Locate every blood parasite and identify its species.
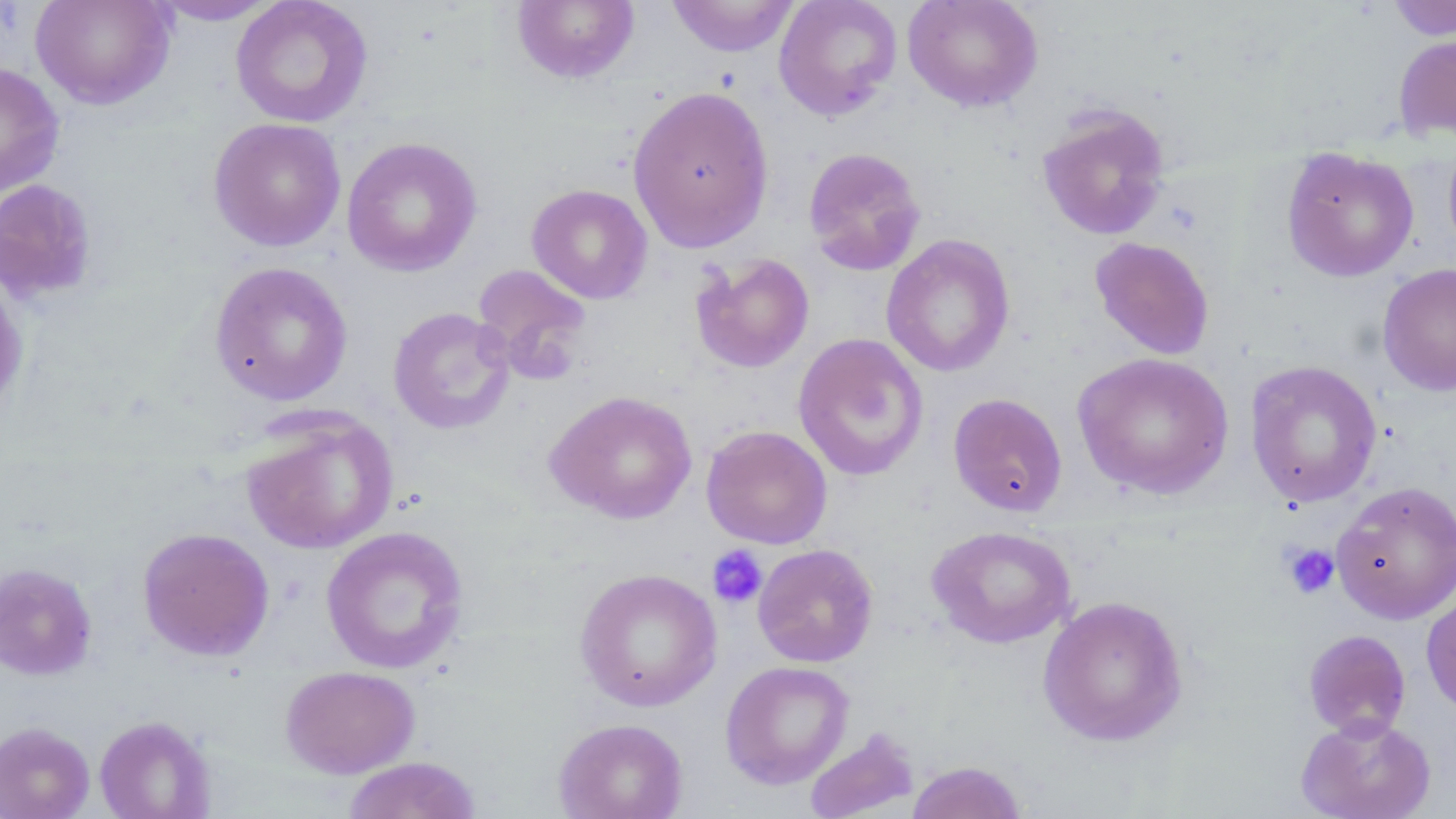

No blood parasites observed.

Approximate bounding boxes as (x1, y1, x2, y2) in pixels. Platelet locations: (1280, 542, 1341, 599), (707, 545, 768, 608). Uninfected red blood cell locations: (31, 0, 176, 109), (146, 0, 285, 25), (231, 0, 372, 128), (666, 0, 800, 58), (773, 0, 902, 121), (903, 0, 1043, 112), (1385, 0, 1456, 41), (511, 1, 639, 84), (1393, 33, 1456, 143), (0, 63, 65, 197), (627, 85, 775, 252), (1036, 104, 1171, 241), (208, 117, 346, 251), (1443, 134, 1456, 261), (341, 137, 483, 277), (803, 147, 926, 276), (1281, 147, 1419, 283), (0, 178, 98, 303), (526, 184, 653, 304), (881, 233, 1016, 377), (1089, 236, 1215, 360), (690, 253, 815, 373), (209, 261, 354, 406), (471, 263, 594, 380), (1377, 263, 1456, 397), (0, 271, 28, 419), (388, 306, 515, 435), (792, 332, 929, 482), (1072, 352, 1235, 500), (1245, 360, 1383, 507), (545, 390, 698, 524), (948, 392, 1068, 517), (238, 409, 399, 554), (701, 425, 833, 549), (1332, 480, 1456, 624), (927, 525, 1076, 649), (320, 526, 470, 674), (137, 527, 275, 662), (752, 543, 879, 668), (0, 562, 98, 680), (574, 567, 723, 712), (1421, 587, 1456, 718), (1037, 595, 1189, 747), (1302, 629, 1412, 739), (720, 660, 854, 790), (280, 665, 420, 778), (1296, 714, 1437, 819), (94, 715, 216, 819), (553, 717, 689, 819), (0, 721, 95, 819), (803, 728, 920, 819), (343, 756, 483, 818), (906, 760, 1028, 819). Slide-level diagnosis: negative for blood parasites. Image is 1456×819 pixels. Optical microscopy. One field of a larger specimen. May-Grünwald-Giemsa-stained preparation. Thin blood film. Captured at 1000x magnification.